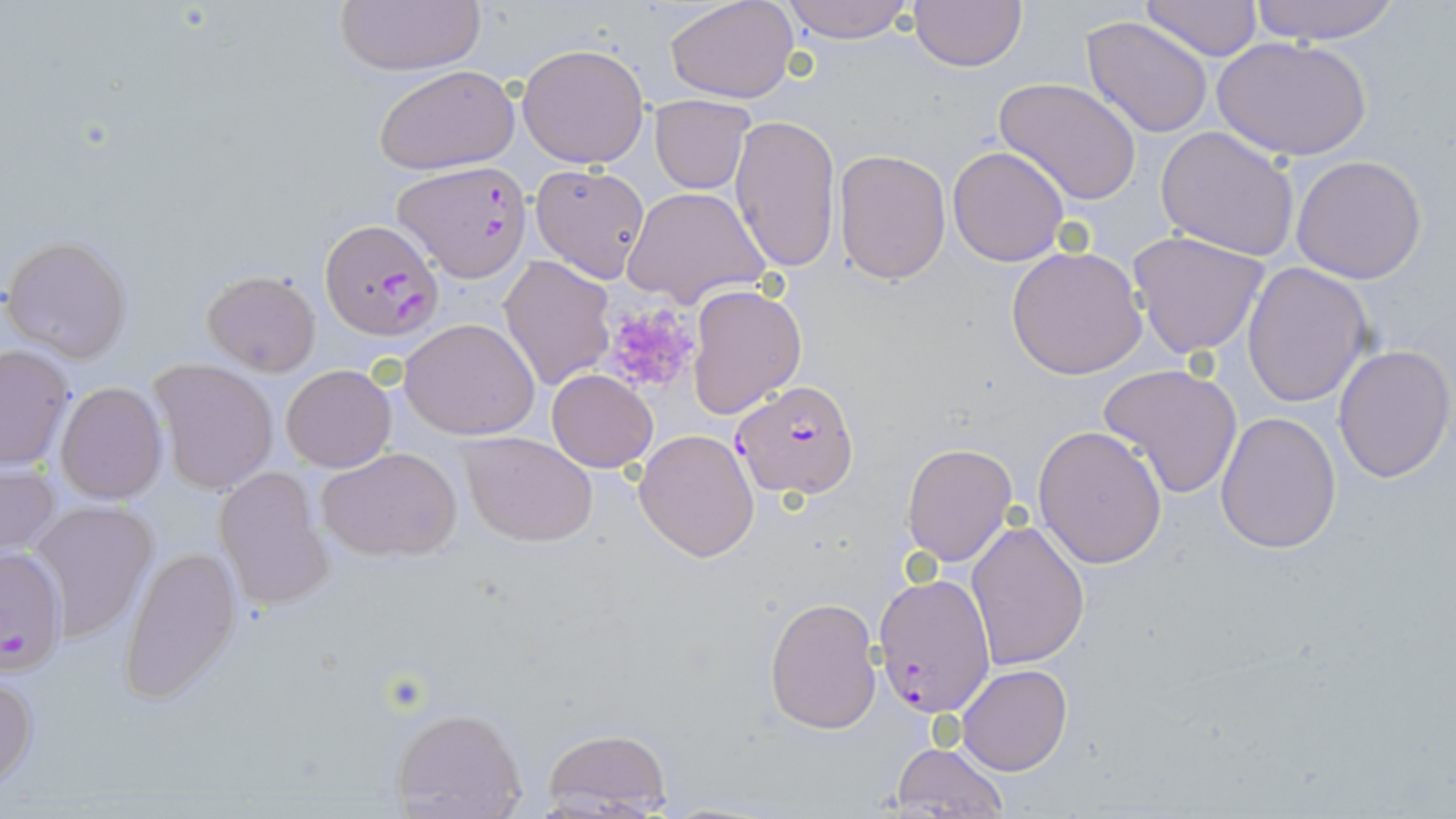

slide-level diagnosis = Plasmodium falciparum
uninfected red blood cell locations = approximate bounding boxes as named x1/y1/x2/y2 corners in pixels: (x1=664, y1=0, x2=801, y2=103), (x1=1136, y1=0, x2=1263, y2=61), (x1=1248, y1=0, x2=1401, y2=44), (x1=333, y1=1, x2=485, y2=76), (x1=776, y1=1, x2=921, y2=44), (x1=907, y1=1, x2=1027, y2=71), (x1=1083, y1=14, x2=1216, y2=138), (x1=1213, y1=36, x2=1372, y2=162), (x1=518, y1=41, x2=651, y2=168), (x1=372, y1=64, x2=519, y2=175), (x1=995, y1=77, x2=1143, y2=205), (x1=648, y1=94, x2=755, y2=194), (x1=729, y1=112, x2=841, y2=272), (x1=1156, y1=125, x2=1300, y2=261), (x1=947, y1=145, x2=1069, y2=266), (x1=833, y1=149, x2=952, y2=286), (x1=1291, y1=155, x2=1427, y2=285), (x1=529, y1=163, x2=651, y2=284), (x1=623, y1=186, x2=770, y2=308), (x1=1127, y1=229, x2=1274, y2=360), (x1=4, y1=234, x2=132, y2=363), (x1=1006, y1=246, x2=1148, y2=380), (x1=499, y1=256, x2=614, y2=391), (x1=1241, y1=261, x2=1372, y2=407), (x1=202, y1=270, x2=321, y2=375), (x1=685, y1=282, x2=807, y2=420), (x1=401, y1=317, x2=542, y2=440), (x1=0, y1=342, x2=77, y2=471), (x1=1333, y1=344, x2=1455, y2=484), (x1=149, y1=358, x2=279, y2=495), (x1=279, y1=362, x2=396, y2=472), (x1=1099, y1=363, x2=1243, y2=500), (x1=547, y1=368, x2=659, y2=474), (x1=54, y1=382, x2=168, y2=504), (x1=1214, y1=409, x2=1343, y2=554), (x1=1033, y1=424, x2=1167, y2=568), (x1=634, y1=429, x2=761, y2=562), (x1=459, y1=431, x2=598, y2=546), (x1=901, y1=443, x2=1018, y2=566), (x1=318, y1=447, x2=463, y2=562), (x1=0, y1=458, x2=60, y2=560), (x1=213, y1=465, x2=333, y2=612), (x1=27, y1=499, x2=158, y2=642), (x1=966, y1=521, x2=1091, y2=671), (x1=120, y1=544, x2=240, y2=702), (x1=764, y1=596, x2=883, y2=734), (x1=957, y1=665, x2=1071, y2=775), (x1=0, y1=666, x2=38, y2=791), (x1=389, y1=706, x2=529, y2=819), (x1=538, y1=728, x2=675, y2=817), (x1=889, y1=739, x2=1010, y2=818)
platelet locations = approximate bounding boxes as named x1/y1/x2/y2 corners in pixels: (x1=598, y1=301, x2=702, y2=396)
Plasmodium falciparum-infected red blood cell locations = approximate bounding boxes as named x1/y1/x2/y2 corners in pixels: (x1=395, y1=160, x2=532, y2=281), (x1=321, y1=217, x2=442, y2=341), (x1=731, y1=378, x2=858, y2=500), (x1=0, y1=544, x2=68, y2=679), (x1=871, y1=573, x2=997, y2=719)
magnification = 1000x
stain = May-Grünwald-Giemsa
modality = light microscopy
field of view = single
preparation = thin blood film
image size = 1456×819 pixels